Name the blood parasite species.
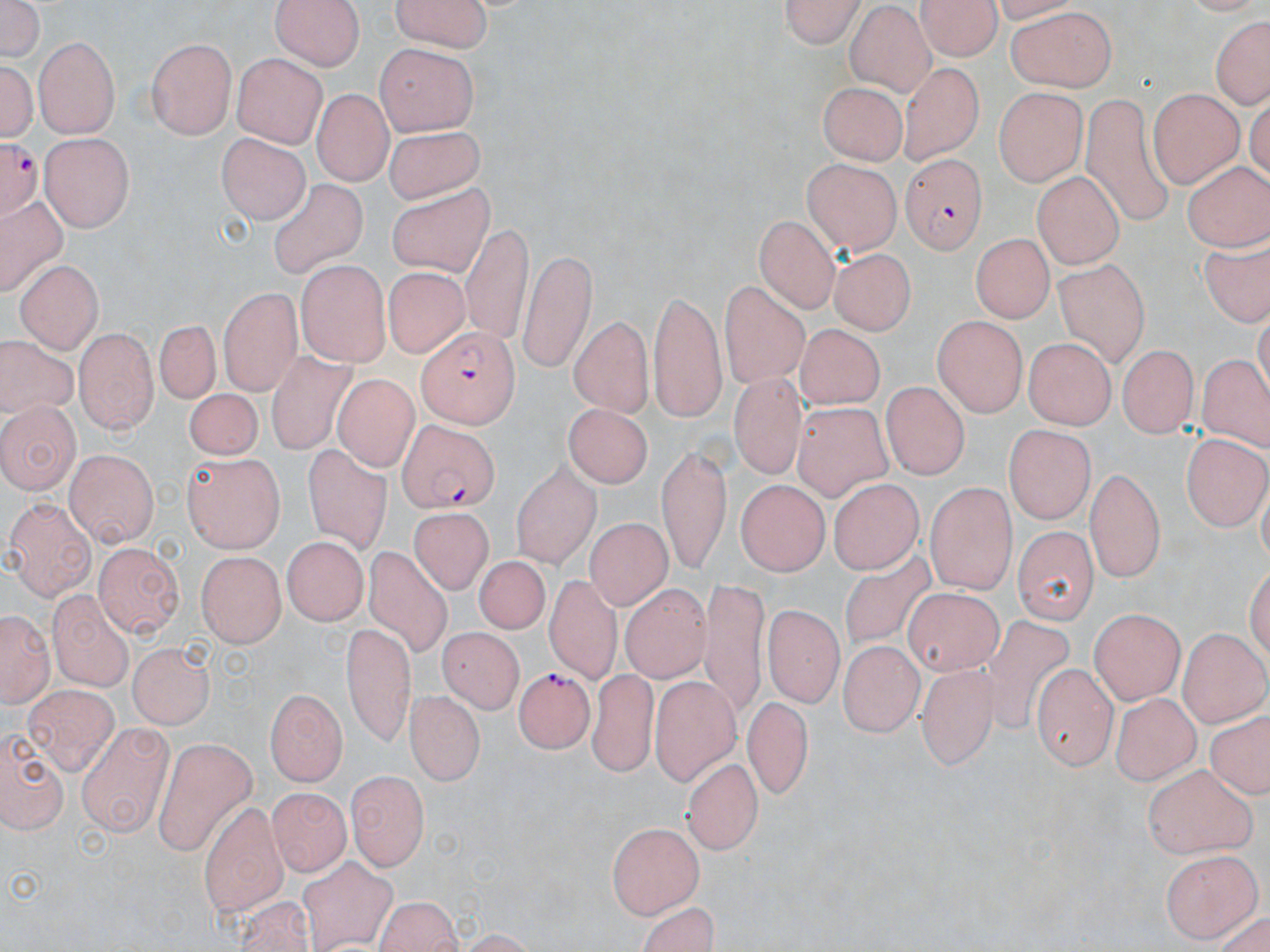
Plasmodium falciparum.

Approximate bounding boxes as [x1, y1, x2, y2] in pixels. Plasmodium falciparum-infected red blood cell locations: [0, 134, 45, 224], [897, 153, 990, 253], [417, 326, 519, 429], [395, 420, 497, 513], [514, 668, 598, 761]. Uninfected red blood cell locations: [1, 0, 45, 63], [269, 0, 366, 68], [392, 0, 496, 54], [779, 0, 863, 51], [920, 0, 999, 63], [1004, 6, 1115, 93], [847, 7, 935, 95], [1208, 17, 1270, 110], [34, 37, 118, 135], [145, 37, 240, 139], [376, 44, 479, 130], [231, 52, 327, 147], [5, 61, 35, 141], [899, 62, 984, 160], [816, 80, 905, 166], [991, 87, 1086, 184], [1151, 88, 1241, 186], [313, 89, 388, 188], [1081, 95, 1173, 230], [380, 123, 486, 202], [39, 132, 135, 231], [215, 132, 308, 222], [801, 160, 902, 252], [1182, 161, 1270, 257], [1032, 170, 1126, 268], [269, 180, 371, 280], [386, 180, 487, 273], [1, 199, 70, 303], [754, 215, 838, 312], [460, 225, 535, 344], [971, 231, 1055, 321], [831, 245, 914, 336], [1198, 245, 1270, 333], [521, 248, 598, 371], [16, 258, 105, 352], [297, 261, 390, 368], [1051, 261, 1148, 370], [385, 266, 469, 359], [721, 280, 814, 395], [216, 286, 301, 395], [646, 292, 725, 424], [933, 314, 1026, 416], [568, 317, 655, 414], [153, 320, 229, 410], [793, 323, 889, 406], [76, 327, 156, 434], [0, 333, 79, 424], [1022, 339, 1116, 429], [1121, 344, 1194, 436], [269, 350, 355, 456], [1198, 353, 1270, 454], [728, 373, 802, 483], [334, 374, 425, 473], [881, 385, 967, 478], [183, 387, 263, 463], [789, 401, 896, 504], [0, 402, 77, 491], [563, 405, 652, 487], [1001, 422, 1098, 517], [1185, 429, 1267, 533], [302, 440, 397, 558], [655, 447, 736, 571], [181, 448, 287, 553], [62, 451, 160, 547], [513, 462, 597, 566], [1087, 466, 1167, 583], [828, 477, 925, 577], [735, 480, 830, 574], [925, 482, 1018, 592], [6, 496, 93, 600], [411, 508, 489, 596], [585, 515, 669, 611], [1011, 525, 1096, 622], [282, 534, 364, 629], [95, 541, 182, 637], [361, 549, 452, 659], [197, 550, 286, 643], [838, 552, 934, 653], [476, 556, 556, 636], [546, 572, 630, 673], [697, 576, 777, 718], [619, 581, 715, 692], [45, 585, 135, 688], [905, 586, 1010, 682], [764, 604, 843, 705], [1089, 607, 1186, 703], [1, 610, 49, 708], [978, 614, 1075, 737], [343, 623, 412, 743], [437, 627, 523, 714], [1180, 630, 1268, 724], [837, 637, 922, 736], [129, 642, 214, 730], [1033, 660, 1117, 768], [917, 663, 1002, 769], [585, 666, 667, 778], [652, 675, 742, 784], [24, 686, 118, 778], [404, 686, 481, 779], [265, 688, 347, 780], [1114, 689, 1197, 786], [741, 694, 817, 800], [1203, 712, 1270, 801], [78, 722, 175, 836], [0, 723, 70, 834], [156, 738, 259, 851], [683, 755, 762, 856], [1142, 762, 1257, 859], [348, 769, 427, 872], [270, 785, 346, 879], [199, 798, 289, 913], [607, 821, 705, 917], [1160, 850, 1258, 940], [298, 854, 399, 952], [234, 894, 312, 952], [371, 894, 466, 952], [643, 899, 724, 952]. Thin blood film. Captured at 1000x magnification. Single field of view. Optical microscopy. May-Grünwald-Giemsa-stained preparation. Image is 1270×952 pixels.